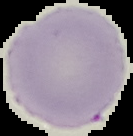

Summary:
  - Result: negative for Plasmodium parasites
  - Image type: segmented cell region with the area outside set to black
  - Image size: 133×136 pixels
  - Preparation: thin blood film